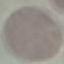
result: no malaria parasites detected
image_type: cell patch, automatically extracted from a larger field of view and resized to 64 × 64 pixels
preparation: thin blood film
capture: smartphone camera at the microscope eyepiece
stain: Giemsa